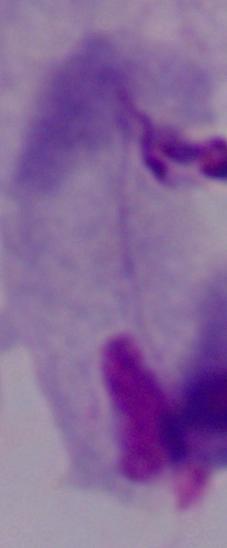
A trichomonad is shown. Photomicrograph. Captured at 1000x magnification.